Assess this cell for malaria.
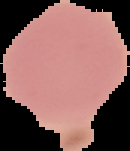

Uninfected.

Summary:
  - Image size: 130×151 pixels
  - Preparation: thin blood smear
  - Image type: segmented cell region with the area outside set to black